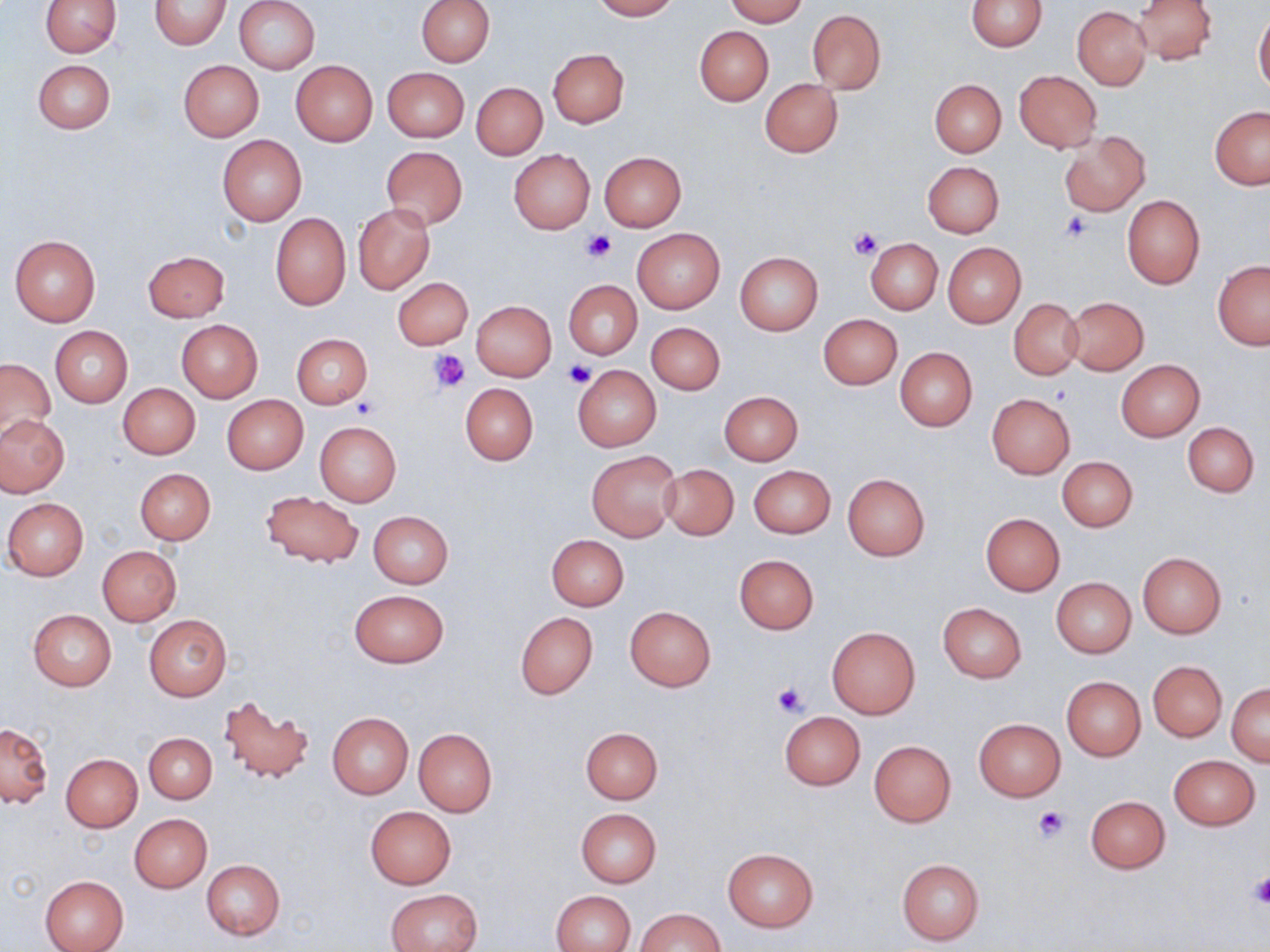 Approximate bounding boxes as (x1, y1, x2, y2) in pixels. Uninfected red blood cell locations: (41, 0, 121, 57), (149, 0, 231, 49), (234, 0, 320, 73), (417, 0, 495, 66), (593, 0, 679, 20), (724, 0, 806, 25), (1133, 0, 1215, 64), (966, 1, 1047, 51), (1072, 6, 1151, 89), (807, 10, 885, 94), (1254, 10, 1270, 92), (695, 26, 773, 105), (548, 49, 629, 127), (32, 58, 116, 134), (178, 59, 264, 142), (290, 60, 378, 145), (382, 67, 470, 142), (1014, 71, 1103, 153), (759, 79, 842, 158), (930, 80, 1005, 156), (472, 83, 547, 159), (1209, 107, 1270, 190), (1058, 130, 1151, 216), (218, 136, 306, 225), (380, 147, 468, 229), (509, 150, 595, 232), (599, 152, 686, 230), (923, 161, 1005, 237), (1121, 194, 1205, 290), (353, 204, 434, 294), (270, 213, 351, 311), (632, 228, 725, 313), (9, 234, 102, 327), (866, 239, 942, 314), (942, 242, 1026, 326), (143, 250, 230, 322), (734, 251, 823, 334), (1213, 261, 1270, 350), (392, 277, 472, 349), (563, 280, 642, 359), (1064, 297, 1148, 375), (1009, 299, 1082, 379), (472, 300, 556, 381), (819, 314, 901, 389), (177, 320, 263, 402), (646, 322, 726, 396), (50, 326, 132, 407), (291, 333, 372, 408), (894, 346, 978, 430), (0, 357, 56, 442), (1116, 360, 1205, 441), (572, 366, 661, 451), (117, 382, 200, 459), (460, 383, 538, 465), (719, 391, 803, 466), (986, 393, 1075, 479), (222, 395, 308, 474), (0, 413, 68, 497), (314, 420, 401, 506), (1183, 421, 1259, 496), (587, 450, 681, 542), (1058, 456, 1138, 532), (661, 465, 738, 540), (747, 465, 836, 539), (135, 468, 216, 544), (842, 474, 930, 562), (260, 489, 365, 570), (3, 498, 89, 579), (368, 510, 452, 588), (980, 513, 1065, 596), (546, 534, 629, 609), (97, 545, 182, 626), (1137, 552, 1226, 639), (733, 554, 818, 634), (1051, 577, 1136, 658), (350, 589, 449, 668), (938, 602, 1026, 682), (624, 605, 715, 691), (28, 609, 116, 691), (515, 612, 597, 700), (144, 614, 231, 701), (827, 626, 920, 718), (1148, 661, 1226, 741), (1061, 676, 1145, 760), (1227, 683, 1270, 766), (217, 694, 314, 785), (326, 712, 414, 799), (779, 712, 865, 790), (973, 717, 1065, 800), (1, 722, 52, 807), (580, 727, 663, 803), (413, 728, 498, 815), (144, 732, 217, 803), (868, 740, 955, 827), (61, 753, 142, 831), (1169, 755, 1260, 830), (1085, 795, 1171, 873), (364, 806, 457, 888), (575, 808, 661, 887), (129, 814, 212, 893), (723, 848, 818, 931), (201, 858, 285, 941), (896, 858, 984, 945), (40, 875, 128, 952), (386, 888, 483, 952), (549, 890, 635, 952), (637, 907, 725, 952). Platelet locations: (1061, 212, 1092, 242), (849, 226, 884, 260), (580, 231, 617, 262), (428, 350, 469, 394), (563, 361, 595, 389), (353, 398, 383, 421), (773, 681, 808, 718), (1033, 806, 1068, 841), (1247, 869, 1268, 906). Slide-level diagnosis: no evidence of blood parasites. Thin blood film. Single field of view. May-Grünwald-Giemsa stain. Image is 1270×952 pixels. Optical microscopy. 1000x magnification.